Comment on the morphology of the red blood cells.
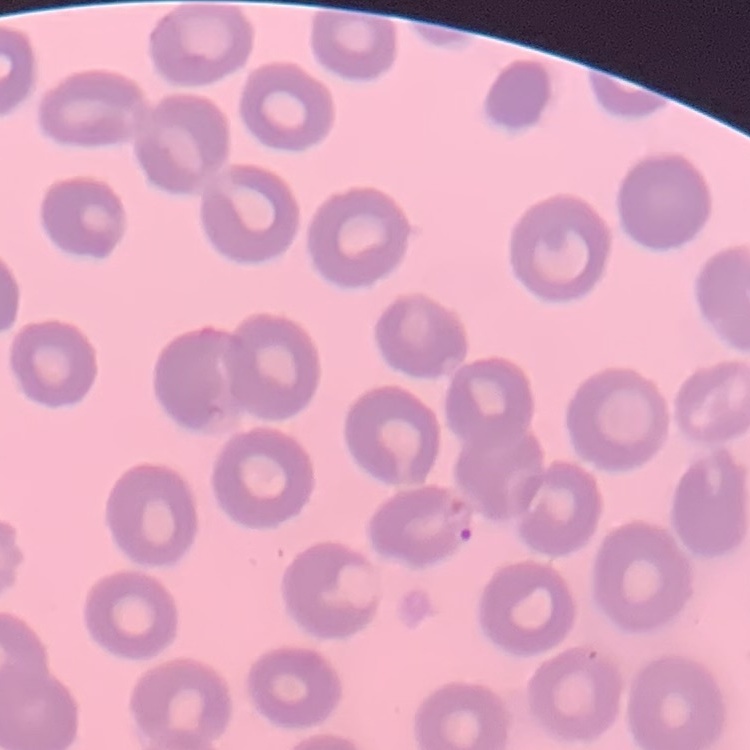
No rouleaux formation.

Summary:
  - Preparation: thin blood smear
  - Stain: Field's or Giemsa
  - Image type: square crop of a larger photomicrograph